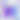
Summary:
  - Identification: Toxoplasma gondii
  - Magnification: 400x
  - Modality: photomicrograph